Locate platelets.
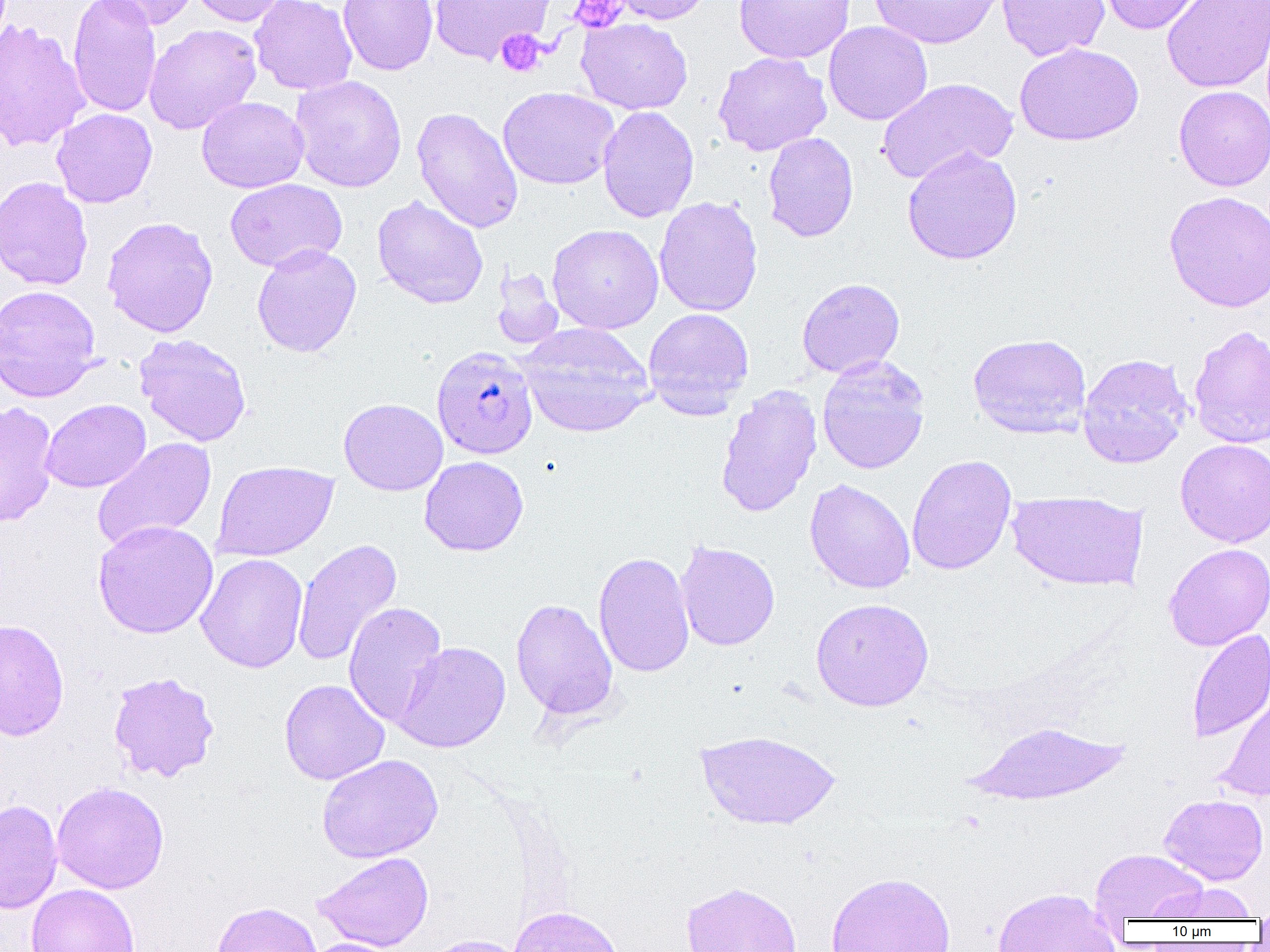

Approximate bounding boxes as named x1/y1/x2/y2 corners in pixels.
Platelets: (x1=569, y1=1, x2=628, y2=33), (x1=496, y1=29, x2=547, y2=77).

Uninfected red blood cell locations: (x1=68, y1=0, x2=162, y2=118), (x1=90, y1=0, x2=200, y2=31), (x1=188, y1=0, x2=289, y2=27), (x1=250, y1=0, x2=357, y2=95), (x1=338, y1=0, x2=438, y2=76), (x1=429, y1=0, x2=554, y2=65), (x1=607, y1=0, x2=713, y2=25), (x1=734, y1=0, x2=855, y2=63), (x1=868, y1=0, x2=1005, y2=49), (x1=996, y1=0, x2=1110, y2=62), (x1=1096, y1=0, x2=1212, y2=35), (x1=1162, y1=0, x2=1269, y2=94), (x1=576, y1=18, x2=693, y2=114), (x1=0, y1=20, x2=90, y2=153), (x1=823, y1=21, x2=933, y2=125), (x1=144, y1=23, x2=262, y2=134), (x1=1014, y1=43, x2=1144, y2=146), (x1=712, y1=51, x2=832, y2=156), (x1=289, y1=75, x2=407, y2=193), (x1=876, y1=76, x2=1019, y2=184), (x1=1174, y1=85, x2=1270, y2=191), (x1=498, y1=86, x2=619, y2=190), (x1=197, y1=97, x2=309, y2=193), (x1=597, y1=106, x2=699, y2=223), (x1=411, y1=107, x2=523, y2=233), (x1=52, y1=108, x2=157, y2=208), (x1=762, y1=131, x2=859, y2=242), (x1=901, y1=146, x2=1023, y2=265), (x1=0, y1=176, x2=93, y2=291), (x1=224, y1=178, x2=347, y2=272), (x1=1164, y1=190, x2=1270, y2=312), (x1=372, y1=195, x2=489, y2=309), (x1=654, y1=196, x2=763, y2=317), (x1=101, y1=216, x2=219, y2=338), (x1=547, y1=223, x2=664, y2=334), (x1=251, y1=243, x2=362, y2=358), (x1=491, y1=266, x2=565, y2=351), (x1=797, y1=278, x2=905, y2=378), (x1=0, y1=284, x2=101, y2=403), (x1=643, y1=307, x2=754, y2=419), (x1=517, y1=323, x2=654, y2=437), (x1=1188, y1=324, x2=1270, y2=449), (x1=967, y1=332, x2=1091, y2=439), (x1=133, y1=333, x2=252, y2=447), (x1=1077, y1=353, x2=1192, y2=469), (x1=816, y1=355, x2=930, y2=474), (x1=715, y1=384, x2=823, y2=518), (x1=338, y1=398, x2=448, y2=496), (x1=40, y1=399, x2=151, y2=492), (x1=0, y1=400, x2=59, y2=528), (x1=92, y1=437, x2=217, y2=552), (x1=1175, y1=439, x2=1270, y2=547), (x1=907, y1=454, x2=1017, y2=575), (x1=419, y1=456, x2=528, y2=556), (x1=211, y1=460, x2=338, y2=561), (x1=804, y1=479, x2=916, y2=594), (x1=1006, y1=490, x2=1148, y2=592), (x1=93, y1=520, x2=218, y2=639), (x1=292, y1=538, x2=402, y2=667), (x1=676, y1=541, x2=780, y2=651), (x1=1163, y1=543, x2=1270, y2=651), (x1=593, y1=551, x2=694, y2=677), (x1=195, y1=553, x2=308, y2=673), (x1=511, y1=598, x2=618, y2=720), (x1=810, y1=598, x2=933, y2=711), (x1=343, y1=601, x2=447, y2=727), (x1=0, y1=618, x2=69, y2=741), (x1=1186, y1=629, x2=1270, y2=743), (x1=393, y1=641, x2=511, y2=753), (x1=107, y1=671, x2=220, y2=782), (x1=279, y1=678, x2=390, y2=785), (x1=1215, y1=690, x2=1270, y2=802), (x1=968, y1=720, x2=1130, y2=807), (x1=695, y1=729, x2=840, y2=830), (x1=317, y1=753, x2=443, y2=863), (x1=51, y1=781, x2=169, y2=894), (x1=1159, y1=794, x2=1268, y2=885), (x1=0, y1=799, x2=63, y2=913), (x1=1090, y1=849, x2=1208, y2=923), (x1=313, y1=851, x2=434, y2=951), (x1=824, y1=871, x2=956, y2=952), (x1=681, y1=881, x2=802, y2=952), (x1=26, y1=883, x2=139, y2=952), (x1=1151, y1=883, x2=1259, y2=921), (x1=993, y1=887, x2=1119, y2=952), (x1=1254, y1=897, x2=1270, y2=932), (x1=211, y1=901, x2=322, y2=952), (x1=507, y1=905, x2=625, y2=952), (x1=419, y1=934, x2=529, y2=952), (x1=302, y1=937, x2=406, y2=952). Plasmodium falciparum-infected red blood cell locations: (x1=431, y1=346, x2=537, y2=459). Slide-level diagnosis: Plasmodium falciparum. One field of a larger specimen. Optical microscopy. Thin blood film. 1000x magnification. Image is 1270×952 pixels.